Locate the cells, classifying each as a parasitized RBC, an uninfected RBC, or a WBC.
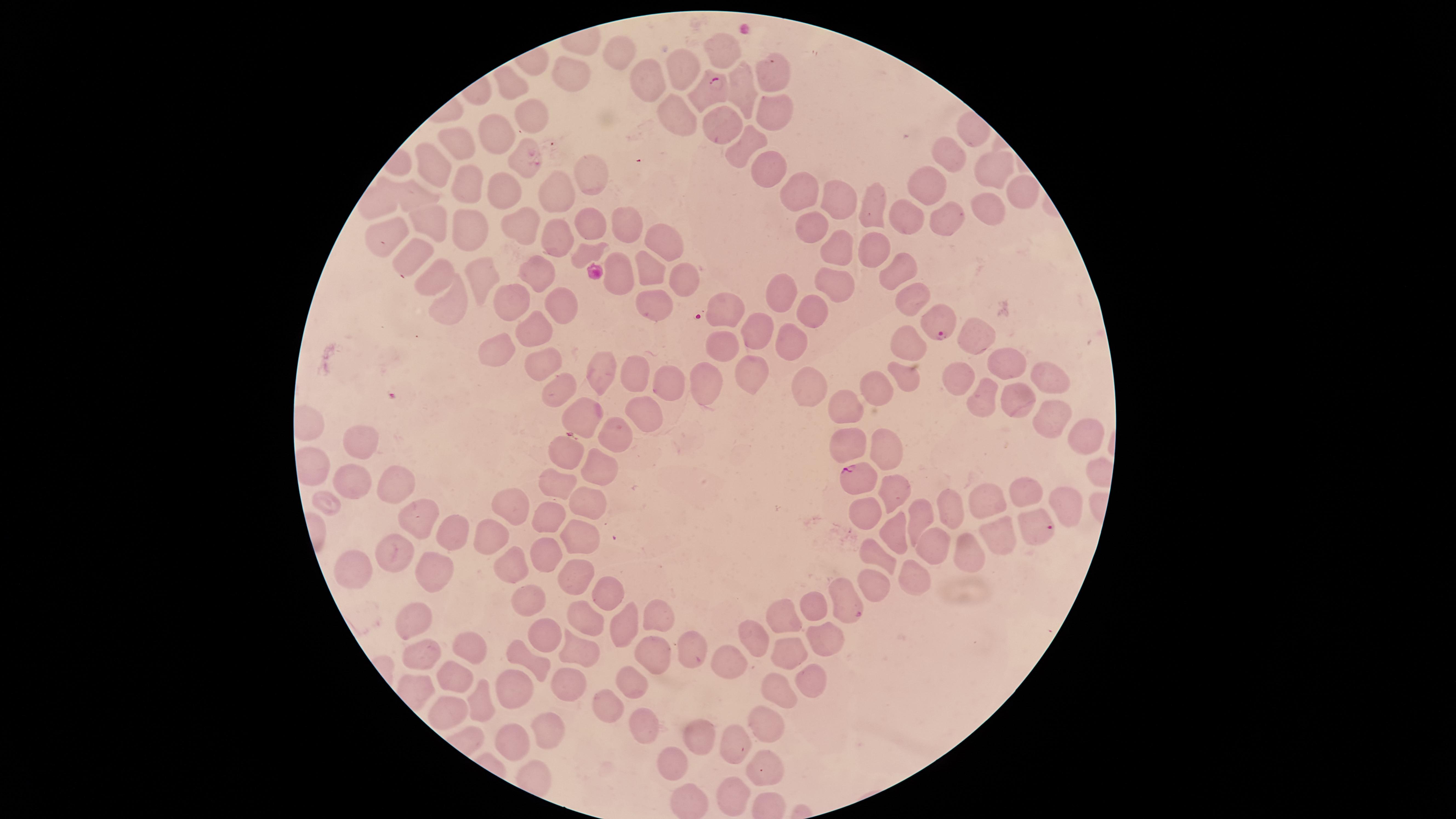

Approximate marker points, in pixels from the top-left corner.
Parasitized RBCs: (x=708, y=84), (x=939, y=321), (x=854, y=478), (x=1036, y=524), (x=849, y=605).
Uninfected RBCs: (x=726, y=49), (x=619, y=53), (x=673, y=71), (x=771, y=71), (x=572, y=75), (x=648, y=81), (x=508, y=82), (x=737, y=91), (x=527, y=115), (x=670, y=115), (x=772, y=115), (x=493, y=129), (x=727, y=130), (x=748, y=140), (x=454, y=145), (x=952, y=155), (x=517, y=159), (x=988, y=165), (x=434, y=167), (x=766, y=168), (x=591, y=175), (x=469, y=184), (x=934, y=186), (x=800, y=191), (x=507, y=192), (x=1021, y=192), (x=416, y=194), (x=554, y=199), (x=377, y=202), (x=839, y=203), (x=874, y=204), (x=987, y=207), (x=907, y=218), (x=943, y=218), (x=428, y=220), (x=588, y=225), (x=470, y=226), (x=520, y=227), (x=807, y=227), (x=387, y=228), (x=627, y=231), (x=557, y=236), (x=664, y=246), (x=583, y=251), (x=864, y=251), (x=413, y=253), (x=834, y=254), (x=897, y=267), (x=538, y=269), (x=648, y=271), (x=614, y=272), (x=434, y=277), (x=481, y=279), (x=684, y=280), (x=830, y=284), (x=783, y=292), (x=909, y=295), (x=516, y=301), (x=728, y=303), (x=650, y=304), (x=562, y=306), (x=445, y=307), (x=812, y=308), (x=758, y=332), (x=530, y=336), (x=975, y=337), (x=792, y=341), (x=720, y=344), (x=915, y=346), (x=498, y=349), (x=1011, y=363), (x=540, y=365), (x=601, y=372), (x=900, y=372), (x=636, y=373), (x=747, y=375), (x=709, y=378), (x=957, y=378), (x=1052, y=379), (x=666, y=383), (x=817, y=386), (x=884, y=386), (x=560, y=388), (x=1015, y=397), (x=851, y=398), (x=986, y=399), (x=645, y=409), (x=579, y=413), (x=1049, y=415), (x=1077, y=439), (x=356, y=441), (x=608, y=441), (x=847, y=442), (x=884, y=449), (x=562, y=458), (x=597, y=471), (x=550, y=480), (x=350, y=483), (x=401, y=485), (x=1030, y=488), (x=993, y=497), (x=891, y=498), (x=330, y=502), (x=1061, y=503), (x=588, y=506), (x=511, y=507), (x=861, y=511), (x=546, y=514), (x=960, y=515), (x=923, y=519), (x=422, y=522), (x=458, y=531), (x=887, y=532), (x=491, y=536), (x=995, y=537), (x=585, y=540), (x=971, y=547), (x=931, y=550), (x=879, y=556), (x=399, y=558), (x=543, y=558), (x=515, y=570), (x=347, y=572), (x=910, y=572), (x=424, y=574), (x=576, y=575), (x=868, y=587), (x=608, y=593), (x=526, y=599), (x=813, y=609), (x=658, y=615), (x=787, y=616), (x=583, y=621), (x=417, y=627), (x=622, y=628), (x=546, y=632), (x=750, y=639), (x=823, y=640), (x=477, y=649), (x=653, y=649), (x=790, y=650), (x=687, y=652), (x=526, y=653), (x=580, y=653), (x=427, y=655), (x=718, y=663), (x=452, y=676), (x=816, y=676), (x=567, y=680), (x=632, y=685), (x=776, y=688), (x=513, y=690), (x=444, y=706), (x=484, y=706), (x=607, y=706), (x=774, y=723), (x=638, y=730), (x=543, y=734), (x=512, y=735), (x=695, y=735), (x=733, y=746), (x=670, y=765), (x=760, y=768), (x=736, y=796).
No WBCs identified.

Giemsa-stained preparation. Smartphone photograph through the microscope eyepiece. Species: Plasmodium falciparum. Thin blood smear. The visible region is circular. Image is 1456×819 pixels. One field of view of the specimen.